State which cell type is depicted.
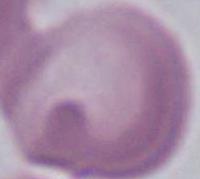

This is an erythrocyte.

Photomicrograph. Captured at 1000x magnification.